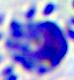 Photomicrograph. Captured at 400x magnification. A leukocyte is shown.